Give the extent of all uninfected red blood cells.
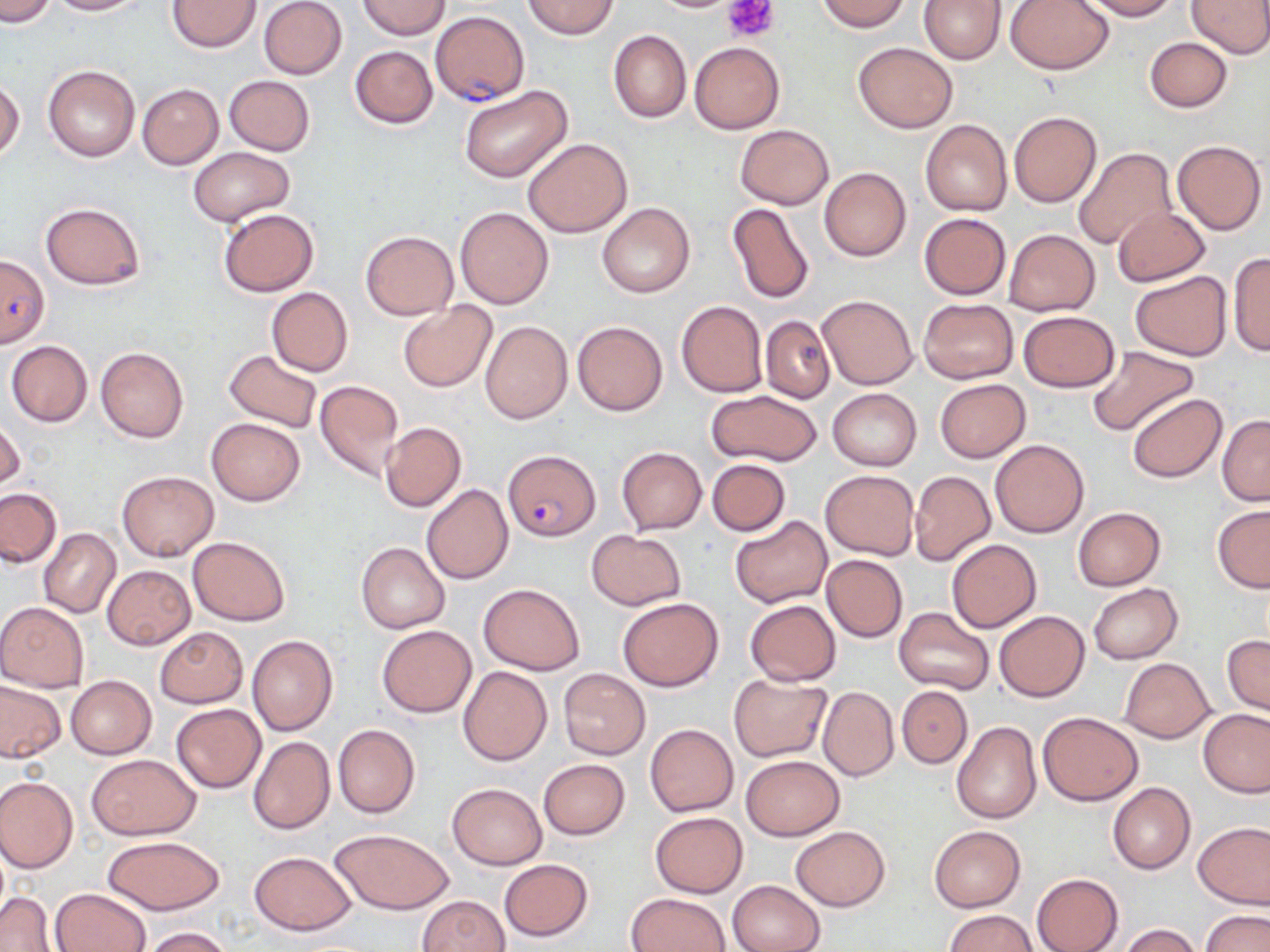

Approximate bounding boxes as (x1,y1)-(x2,y2) corner pairs in pixels.
Uninfected red blood cells: (0,0)-(56,27), (45,0)-(142,15), (167,0)-(261,52), (258,0)-(347,80), (359,0)-(448,39), (522,0)-(618,39), (815,0)-(912,32), (919,0)-(1005,64), (1083,0)-(1180,20), (1188,0)-(1270,58), (1006,1)-(1112,74), (608,30)-(691,123), (1145,38)-(1231,112), (689,41)-(785,133), (853,42)-(957,133), (350,45)-(437,129), (43,66)-(139,162), (224,75)-(315,154), (0,80)-(24,161), (136,83)-(223,168), (458,84)-(573,183), (1008,111)-(1101,208), (920,119)-(1013,216), (735,124)-(834,210), (523,138)-(633,236), (1171,140)-(1266,234), (187,147)-(295,225), (1073,147)-(1177,250), (818,166)-(911,261), (39,202)-(146,290), (597,202)-(695,297), (726,203)-(816,306), (455,206)-(554,310), (1111,207)-(1210,287), (218,209)-(320,296), (920,212)-(1010,299), (1003,229)-(1099,316), (360,230)-(459,320), (1227,252)-(1270,357), (1130,272)-(1233,359), (265,287)-(353,377), (816,294)-(917,389), (918,298)-(1018,384), (676,300)-(768,398), (398,301)-(497,392), (1019,310)-(1120,391), (761,315)-(835,403), (481,320)-(573,423), (572,320)-(667,416), (6,340)-(92,426), (1087,345)-(1199,437), (96,346)-(188,442), (223,349)-(323,435), (934,378)-(1031,463), (314,380)-(405,482), (828,388)-(921,470), (706,389)-(822,467), (1127,393)-(1227,483), (1217,414)-(1270,506), (206,418)-(304,505), (1,419)-(25,492), (379,422)-(466,511), (990,439)-(1090,537), (617,446)-(708,534), (707,459)-(790,536), (116,469)-(219,562), (821,469)-(918,560), (909,470)-(995,566), (421,484)-(513,584), (0,488)-(61,568), (1212,504)-(1270,593), (1072,506)-(1165,591), (729,515)-(834,608), (39,528)-(120,617), (587,530)-(685,610), (188,536)-(290,626), (946,539)-(1041,632), (355,542)-(449,634), (820,554)-(907,642), (102,565)-(195,649), (478,583)-(584,675), (1089,584)-(1183,663), (617,597)-(724,692), (745,599)-(842,686), (0,601)-(89,692), (893,607)-(994,694), (995,611)-(1089,701), (377,624)-(476,717), (155,627)-(247,707), (1223,634)-(1269,715), (247,636)-(337,736), (1120,657)-(1215,742), (459,666)-(551,765), (558,669)-(650,759), (728,673)-(833,763), (66,675)-(156,759), (0,681)-(65,762), (817,685)-(898,782), (897,686)-(971,767), (171,704)-(265,792), (1198,708)-(1269,798), (1038,713)-(1142,805), (951,721)-(1041,823), (333,723)-(421,819), (645,724)-(738,816), (248,736)-(335,835), (88,753)-(200,839), (741,754)-(843,840), (537,758)-(630,839), (0,776)-(78,872), (1107,782)-(1196,875), (446,783)-(546,870), (649,811)-(747,898), (1194,820)-(1270,909), (929,824)-(1026,912), (790,826)-(889,911), (329,828)-(455,913), (103,835)-(223,915), (249,850)-(356,935), (498,859)-(593,941), (1031,873)-(1123,952), (728,879)-(824,952), (52,889)-(151,952), (0,892)-(55,951), (627,892)-(730,952), (416,895)-(510,952), (1199,909)-(1269,952), (944,910)-(1039,952), (1120,924)-(1202,952), (138,926)-(235,952).

Plasmodium falciparum-infected red blood cell locations: (431,10)-(528,107), (0,255)-(50,347), (504,448)-(599,542). Platelet locations: (726,0)-(779,42). Slide-level diagnosis: Plasmodium falciparum. Thin blood film. Image is 1270×952 pixels. Light microscopy. May-Grünwald-Giemsa stain. Captured at 1000x magnification. Single field of view.